Name the cell type shown.
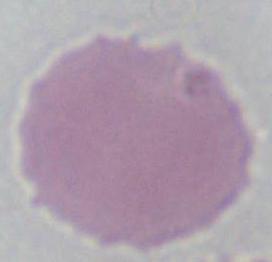
This is an erythrocyte.

Micrograph. 1000x magnification.